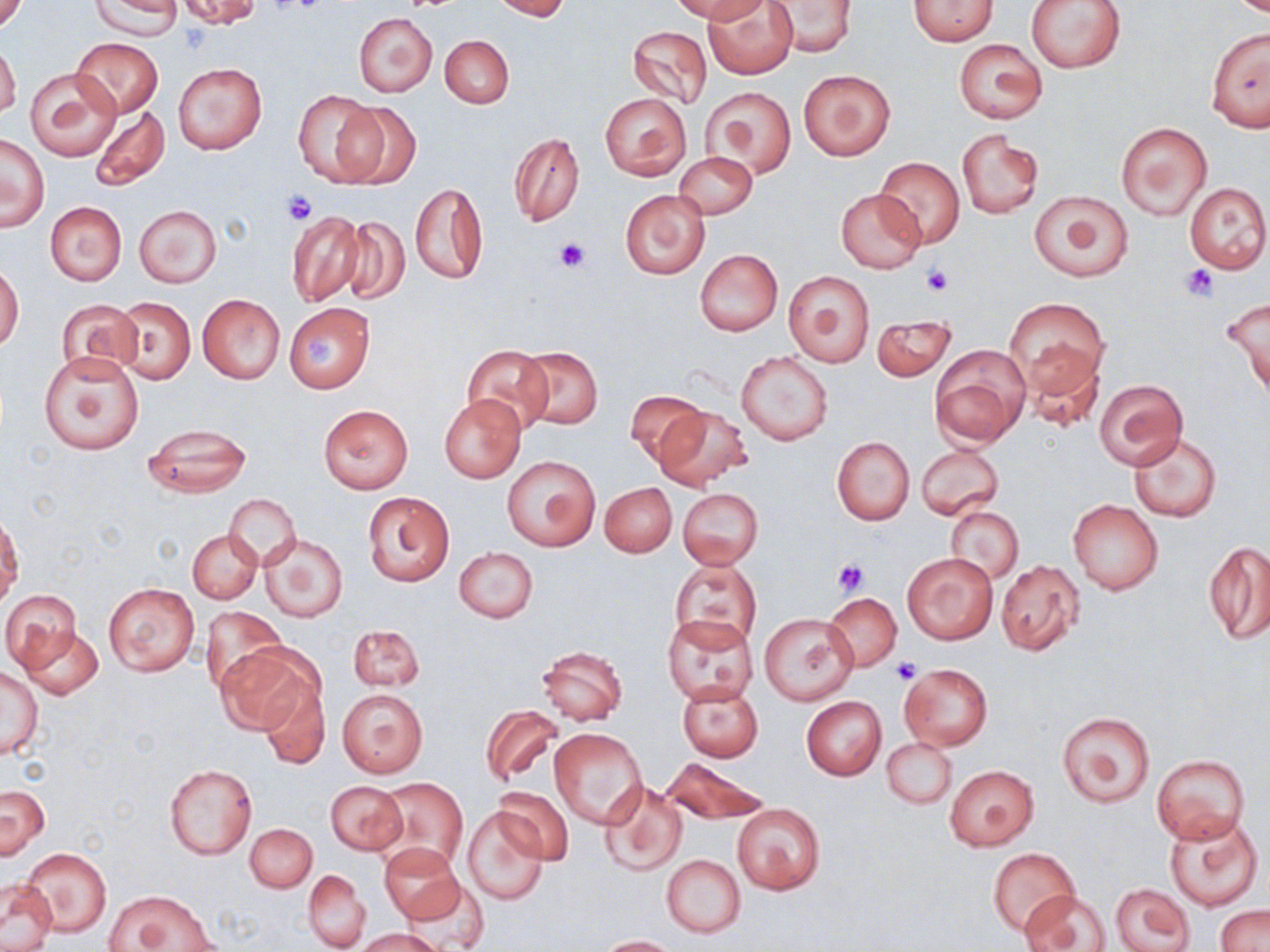
Approximate bounding boxes as named x1/y1/x2/y2 corners in pixels. Uninfected red blood cell locations: (x1=92, y1=0, x2=181, y2=39), (x1=176, y1=0, x2=262, y2=29), (x1=490, y1=0, x2=571, y2=20), (x1=673, y1=0, x2=767, y2=24), (x1=703, y1=0, x2=798, y2=78), (x1=909, y1=0, x2=997, y2=45), (x1=1027, y1=0, x2=1125, y2=73), (x1=0, y1=1, x2=27, y2=35), (x1=766, y1=1, x2=857, y2=57), (x1=353, y1=12, x2=437, y2=97), (x1=627, y1=25, x2=713, y2=108), (x1=1207, y1=27, x2=1270, y2=132), (x1=440, y1=34, x2=513, y2=108), (x1=71, y1=37, x2=164, y2=118), (x1=954, y1=39, x2=1046, y2=124), (x1=0, y1=42, x2=20, y2=119), (x1=174, y1=63, x2=266, y2=155), (x1=26, y1=67, x2=122, y2=160), (x1=798, y1=70, x2=894, y2=160), (x1=703, y1=86, x2=796, y2=180), (x1=292, y1=88, x2=383, y2=186), (x1=599, y1=92, x2=691, y2=181), (x1=337, y1=101, x2=422, y2=192), (x1=89, y1=105, x2=169, y2=191), (x1=1115, y1=122, x2=1212, y2=219), (x1=956, y1=130, x2=1043, y2=219), (x1=508, y1=133, x2=584, y2=227), (x1=1, y1=135, x2=49, y2=232), (x1=674, y1=152, x2=757, y2=220), (x1=875, y1=156, x2=965, y2=247), (x1=1185, y1=181, x2=1269, y2=274), (x1=410, y1=182, x2=487, y2=285), (x1=621, y1=189, x2=710, y2=279), (x1=835, y1=189, x2=926, y2=273), (x1=1029, y1=189, x2=1135, y2=282), (x1=45, y1=201, x2=126, y2=285), (x1=134, y1=205, x2=223, y2=288), (x1=285, y1=209, x2=367, y2=308), (x1=336, y1=215, x2=410, y2=304), (x1=694, y1=249, x2=783, y2=335), (x1=0, y1=264, x2=23, y2=351), (x1=783, y1=270, x2=875, y2=367), (x1=197, y1=293, x2=285, y2=384), (x1=1220, y1=296, x2=1270, y2=398), (x1=113, y1=297, x2=195, y2=383), (x1=1005, y1=297, x2=1108, y2=393), (x1=56, y1=298, x2=141, y2=379), (x1=284, y1=303, x2=375, y2=392), (x1=871, y1=316, x2=956, y2=382), (x1=928, y1=344, x2=1030, y2=446), (x1=463, y1=345, x2=554, y2=436), (x1=516, y1=346, x2=604, y2=430), (x1=1022, y1=346, x2=1104, y2=435), (x1=736, y1=351, x2=834, y2=446), (x1=37, y1=352, x2=144, y2=455), (x1=1094, y1=378, x2=1187, y2=469), (x1=625, y1=392, x2=708, y2=464), (x1=438, y1=395, x2=526, y2=484), (x1=319, y1=404, x2=412, y2=493), (x1=654, y1=406, x2=753, y2=491), (x1=140, y1=423, x2=253, y2=497), (x1=1128, y1=432, x2=1220, y2=521), (x1=831, y1=436, x2=914, y2=524), (x1=916, y1=443, x2=1004, y2=519), (x1=502, y1=456, x2=599, y2=550), (x1=600, y1=483, x2=676, y2=557), (x1=677, y1=488, x2=762, y2=569), (x1=363, y1=492, x2=454, y2=587), (x1=224, y1=493, x2=300, y2=568), (x1=1067, y1=498, x2=1164, y2=595), (x1=946, y1=506, x2=1023, y2=585), (x1=1, y1=515, x2=23, y2=605), (x1=187, y1=529, x2=262, y2=603), (x1=258, y1=532, x2=347, y2=623), (x1=1204, y1=540, x2=1270, y2=647), (x1=455, y1=547, x2=538, y2=623), (x1=903, y1=553, x2=997, y2=644), (x1=995, y1=559, x2=1084, y2=655), (x1=671, y1=560, x2=761, y2=649), (x1=103, y1=583, x2=201, y2=677), (x1=2, y1=590, x2=81, y2=672), (x1=825, y1=592, x2=901, y2=670), (x1=198, y1=605, x2=287, y2=697), (x1=760, y1=612, x2=858, y2=706), (x1=662, y1=613, x2=757, y2=704), (x1=348, y1=625, x2=424, y2=691), (x1=18, y1=627, x2=104, y2=700), (x1=215, y1=643, x2=318, y2=738), (x1=534, y1=644, x2=628, y2=725), (x1=898, y1=663, x2=993, y2=749), (x1=1, y1=667, x2=44, y2=758), (x1=256, y1=677, x2=329, y2=769), (x1=675, y1=680, x2=764, y2=762), (x1=336, y1=686, x2=429, y2=779), (x1=802, y1=696, x2=886, y2=780), (x1=482, y1=705, x2=564, y2=787), (x1=1057, y1=712, x2=1156, y2=808), (x1=549, y1=728, x2=648, y2=830), (x1=883, y1=738, x2=956, y2=809), (x1=1151, y1=752, x2=1251, y2=843), (x1=663, y1=757, x2=768, y2=824), (x1=163, y1=763, x2=256, y2=860), (x1=944, y1=764, x2=1040, y2=850), (x1=373, y1=778, x2=468, y2=872), (x1=326, y1=780, x2=408, y2=855), (x1=598, y1=780, x2=687, y2=876), (x1=1, y1=785, x2=49, y2=859), (x1=495, y1=787, x2=574, y2=865), (x1=732, y1=802, x2=826, y2=895), (x1=462, y1=809, x2=547, y2=904), (x1=1164, y1=811, x2=1263, y2=912), (x1=246, y1=823, x2=317, y2=892), (x1=378, y1=843, x2=464, y2=926), (x1=22, y1=847, x2=111, y2=938), (x1=989, y1=847, x2=1080, y2=938), (x1=661, y1=854, x2=745, y2=937), (x1=304, y1=870, x2=370, y2=952), (x1=406, y1=876, x2=487, y2=950), (x1=0, y1=881, x2=58, y2=951), (x1=1110, y1=884, x2=1193, y2=950), (x1=107, y1=889, x2=215, y2=952), (x1=1020, y1=889, x2=1111, y2=952), (x1=1215, y1=904, x2=1269, y2=952), (x1=356, y1=929, x2=442, y2=951), (x1=597, y1=935, x2=680, y2=952). Platelet locations: (x1=178, y1=24, x2=211, y2=56), (x1=281, y1=189, x2=319, y2=225), (x1=555, y1=237, x2=591, y2=273), (x1=1183, y1=263, x2=1220, y2=301), (x1=921, y1=265, x2=953, y2=296), (x1=305, y1=338, x2=338, y2=366), (x1=833, y1=558, x2=870, y2=596), (x1=891, y1=657, x2=923, y2=684). Slide-level diagnosis: negative for blood parasites. Image is 1270×952 pixels. Optical microscopy. 1000x magnification. May-Grünwald-Giemsa stain. Thin blood smear. Single field of view.